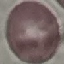 Result: negative for malaria parasites. Photographed with a smartphone camera at the microscope eyepiece. Thin blood film. Cell patch, automatically extracted from a larger field of view and resized to 64 × 64 pixels. Giemsa stain.